Locate every blood parasite and identify its species.
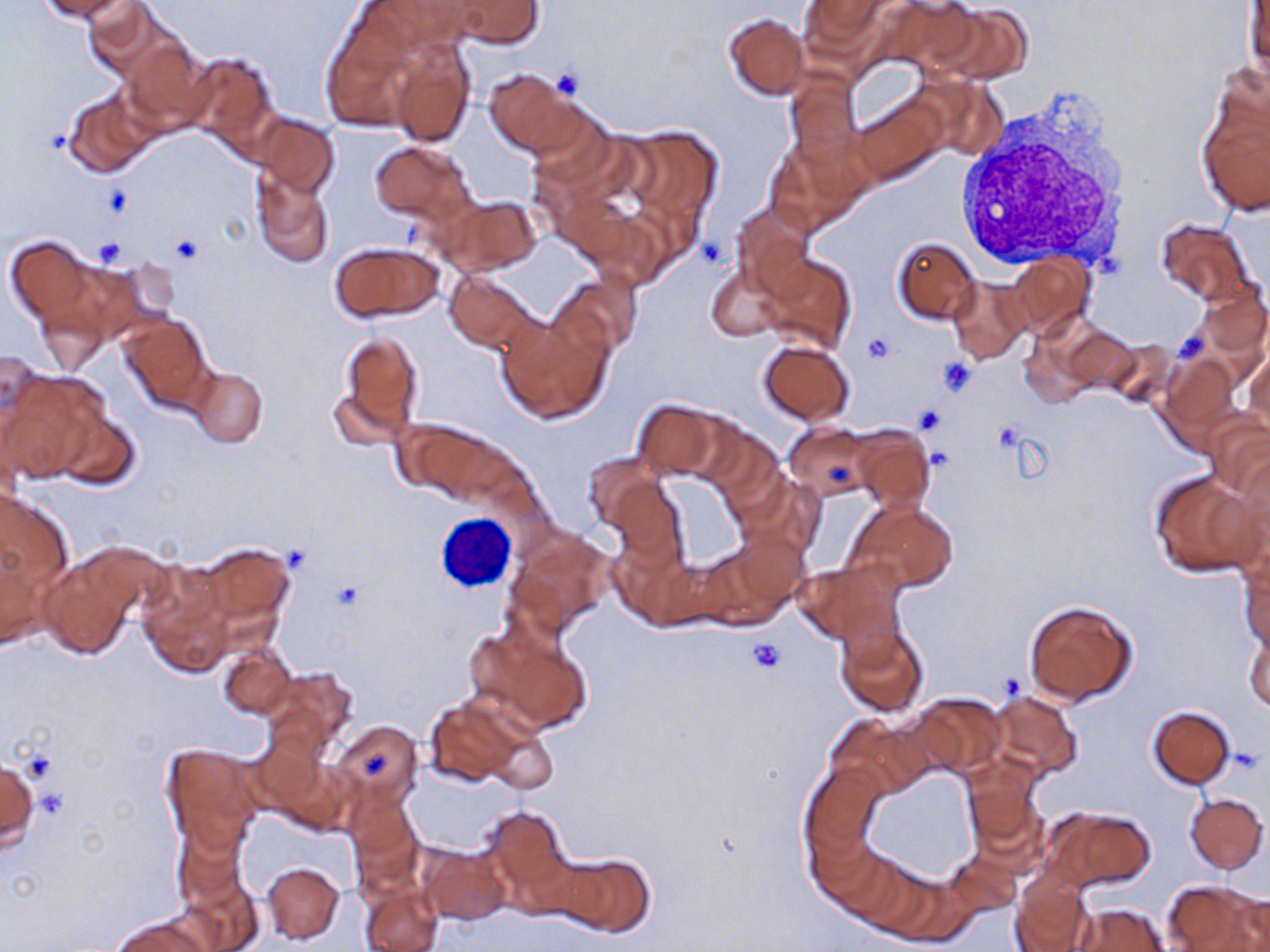

No blood parasites seen.

Summary:
  - Coordinate format: approximate bounding boxes as (x1, y1, x2, y2) in pixels
  - White blood cell locations: (954, 94, 1137, 278)
  - Platelet locations: (552, 67, 585, 98), (41, 125, 69, 153), (102, 186, 133, 217), (171, 233, 203, 265), (93, 237, 126, 267), (1173, 330, 1209, 364), (862, 332, 895, 364), (937, 357, 977, 396), (914, 404, 949, 436), (282, 544, 311, 573), (331, 582, 365, 612), (746, 636, 785, 673), (995, 672, 1026, 701), (1227, 748, 1263, 773), (25, 749, 58, 783), (361, 750, 393, 777)
  - Uninfected red blood cell locations: (37, 0, 136, 23), (452, 0, 544, 49), (800, 0, 889, 52), (84, 2, 176, 82), (1245, 3, 1269, 82), (927, 4, 1032, 83), (723, 13, 810, 99), (319, 22, 427, 133), (120, 38, 212, 135), (388, 43, 475, 146), (181, 50, 279, 150), (484, 67, 580, 157), (62, 91, 157, 179), (1197, 94, 1269, 218), (853, 98, 948, 184), (250, 114, 341, 198), (618, 125, 726, 243), (370, 142, 475, 226), (252, 171, 334, 269), (442, 195, 540, 276), (732, 206, 814, 298), (1156, 220, 1250, 305), (4, 236, 102, 333), (892, 236, 981, 325), (330, 242, 443, 322), (760, 253, 857, 356), (1006, 255, 1095, 336), (706, 268, 784, 341), (446, 270, 540, 352), (551, 273, 642, 358), (948, 277, 1032, 363), (1194, 284, 1270, 360), (120, 314, 212, 413), (496, 314, 611, 424), (1060, 325, 1138, 397), (336, 330, 423, 440), (758, 338, 854, 425), (1103, 340, 1180, 412), (0, 346, 51, 455), (1245, 350, 1270, 431), (1158, 354, 1240, 443), (188, 368, 267, 448), (3, 372, 104, 483), (330, 389, 405, 452), (631, 400, 724, 480), (56, 411, 143, 490), (1207, 414, 1270, 501), (393, 415, 508, 502), (703, 423, 786, 510), (784, 423, 875, 500), (850, 427, 934, 513), (583, 455, 666, 532), (1150, 471, 1264, 577), (610, 478, 687, 568), (0, 490, 74, 626), (848, 499, 959, 591), (505, 528, 614, 640), (729, 528, 808, 608), (195, 542, 292, 633), (39, 548, 145, 659), (1239, 557, 1269, 653), (794, 560, 904, 646), (138, 571, 233, 676), (1024, 600, 1137, 705), (465, 619, 593, 739), (835, 620, 928, 717), (1244, 627, 1269, 715), (218, 640, 295, 720), (262, 665, 359, 759), (991, 690, 1081, 780), (913, 693, 1006, 778), (425, 695, 530, 787), (1148, 705, 1235, 788), (827, 715, 929, 798), (330, 720, 424, 813), (484, 728, 559, 794), (163, 744, 263, 850), (0, 754, 39, 851), (963, 760, 1044, 859), (798, 763, 884, 877), (1184, 793, 1268, 873), (349, 799, 424, 894), (478, 803, 577, 908), (1042, 805, 1156, 892), (173, 819, 245, 910), (418, 845, 512, 925), (944, 850, 1021, 919), (549, 851, 657, 938), (262, 861, 345, 944), (172, 873, 262, 951), (1012, 875, 1095, 952), (358, 876, 442, 952), (1164, 879, 1266, 952), (1227, 891, 1270, 950), (1070, 903, 1168, 952), (110, 915, 213, 952)
  - Slide-level diagnosis: negative for blood parasites
  - Magnification: 1000x
  - Field of view: single
  - Stain: May-Grünwald-Giemsa
  - Preparation: thin blood film
  - Modality: optical microscopy
  - Image size: 1270×952 pixels